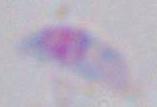

Toxoplasma gondii is shown. Captured at 1000x magnification. Photomicrograph.